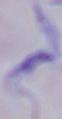

magnification: 1000x
modality: micrograph
identification: trypanosome